Assess this cell for malaria.
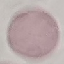
Uninfected.

stain = Giemsa
image type = cell patch, automatically extracted from a larger field of view and resized to 64 × 64 pixels
preparation = thin smear
capture = smartphone through the microscope eyepiece